Outline each Plasmodium falciparum-infected red blood cell.
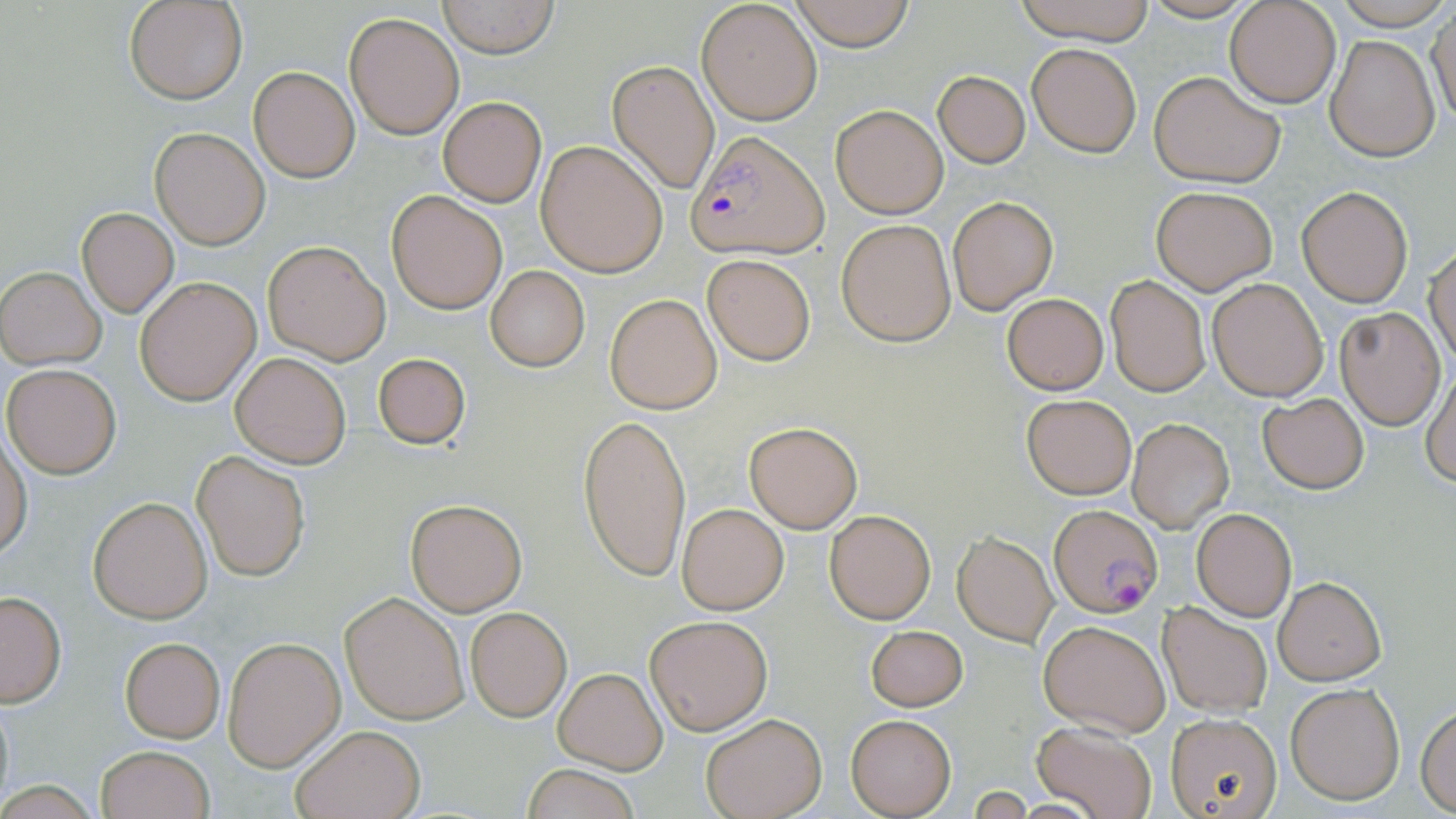
Approximate bounding boxes as named x1/y1/x2/y2 corners in pixels.
Plasmodium falciparum-infected red blood cells: (x1=686, y1=131, x2=829, y2=261), (x1=1049, y1=505, x2=1163, y2=619).

Uninfected red blood cell locations: (x1=126, y1=0, x2=247, y2=104), (x1=788, y1=0, x2=917, y2=50), (x1=1008, y1=0, x2=1160, y2=45), (x1=1224, y1=0, x2=1341, y2=107), (x1=437, y1=1, x2=559, y2=57), (x1=696, y1=2, x2=822, y2=125), (x1=1428, y1=10, x2=1456, y2=126), (x1=345, y1=11, x2=465, y2=140), (x1=1326, y1=36, x2=1440, y2=162), (x1=1027, y1=42, x2=1143, y2=156), (x1=607, y1=59, x2=719, y2=195), (x1=248, y1=66, x2=359, y2=183), (x1=1149, y1=70, x2=1286, y2=187), (x1=934, y1=71, x2=1029, y2=167), (x1=438, y1=96, x2=546, y2=206), (x1=830, y1=103, x2=948, y2=218), (x1=150, y1=128, x2=270, y2=248), (x1=537, y1=141, x2=667, y2=276), (x1=1151, y1=184, x2=1277, y2=295), (x1=1297, y1=186, x2=1412, y2=307), (x1=386, y1=190, x2=506, y2=314), (x1=948, y1=196, x2=1058, y2=315), (x1=77, y1=208, x2=178, y2=317), (x1=837, y1=220, x2=955, y2=345), (x1=262, y1=240, x2=390, y2=364), (x1=1426, y1=243, x2=1456, y2=367), (x1=701, y1=254, x2=816, y2=365), (x1=1, y1=266, x2=106, y2=369), (x1=486, y1=266, x2=589, y2=372), (x1=1106, y1=275, x2=1210, y2=396), (x1=135, y1=276, x2=261, y2=405), (x1=1207, y1=278, x2=1328, y2=401), (x1=1002, y1=292, x2=1109, y2=394), (x1=604, y1=293, x2=722, y2=413), (x1=1336, y1=307, x2=1445, y2=429), (x1=230, y1=351, x2=351, y2=468), (x1=371, y1=351, x2=470, y2=450), (x1=2, y1=363, x2=122, y2=478), (x1=1421, y1=367, x2=1456, y2=488), (x1=1021, y1=394, x2=1136, y2=498), (x1=1258, y1=394, x2=1368, y2=494), (x1=578, y1=414, x2=691, y2=581), (x1=1127, y1=418, x2=1235, y2=533), (x1=744, y1=421, x2=863, y2=533), (x1=0, y1=432, x2=32, y2=560), (x1=192, y1=450, x2=311, y2=581), (x1=87, y1=495, x2=214, y2=623), (x1=405, y1=497, x2=528, y2=616), (x1=677, y1=502, x2=788, y2=615), (x1=1190, y1=506, x2=1297, y2=621), (x1=823, y1=508, x2=937, y2=624), (x1=953, y1=531, x2=1058, y2=646), (x1=1273, y1=575, x2=1385, y2=684), (x1=340, y1=591, x2=470, y2=725), (x1=0, y1=592, x2=66, y2=706), (x1=1157, y1=601, x2=1272, y2=716), (x1=465, y1=607, x2=571, y2=721), (x1=646, y1=614, x2=772, y2=735), (x1=1038, y1=617, x2=1170, y2=737), (x1=865, y1=623, x2=968, y2=712), (x1=118, y1=635, x2=226, y2=742), (x1=223, y1=636, x2=346, y2=771), (x1=553, y1=668, x2=666, y2=775), (x1=1284, y1=681, x2=1406, y2=805), (x1=0, y1=698, x2=14, y2=809), (x1=1416, y1=704, x2=1456, y2=813), (x1=1165, y1=712, x2=1284, y2=819), (x1=700, y1=713, x2=825, y2=819), (x1=845, y1=713, x2=957, y2=817), (x1=1033, y1=722, x2=1158, y2=819), (x1=289, y1=723, x2=425, y2=818), (x1=96, y1=745, x2=214, y2=819), (x1=521, y1=765, x2=642, y2=819). Slide-level diagnosis: Plasmodium falciparum. Captured at 1000x magnification. Single field of view. Thin blood film. Light microscopy. Image is 1456×819 pixels. May-Grünwald-Giemsa stain.